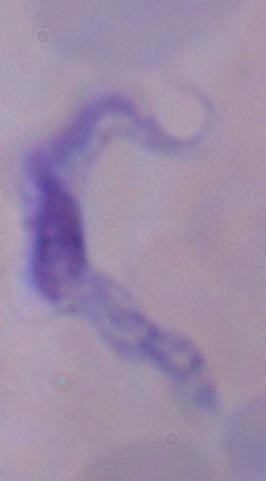
Summary:
  - Magnification: 1000x
  - Identification: trypanosome
  - Modality: micrograph